Locate platelets.
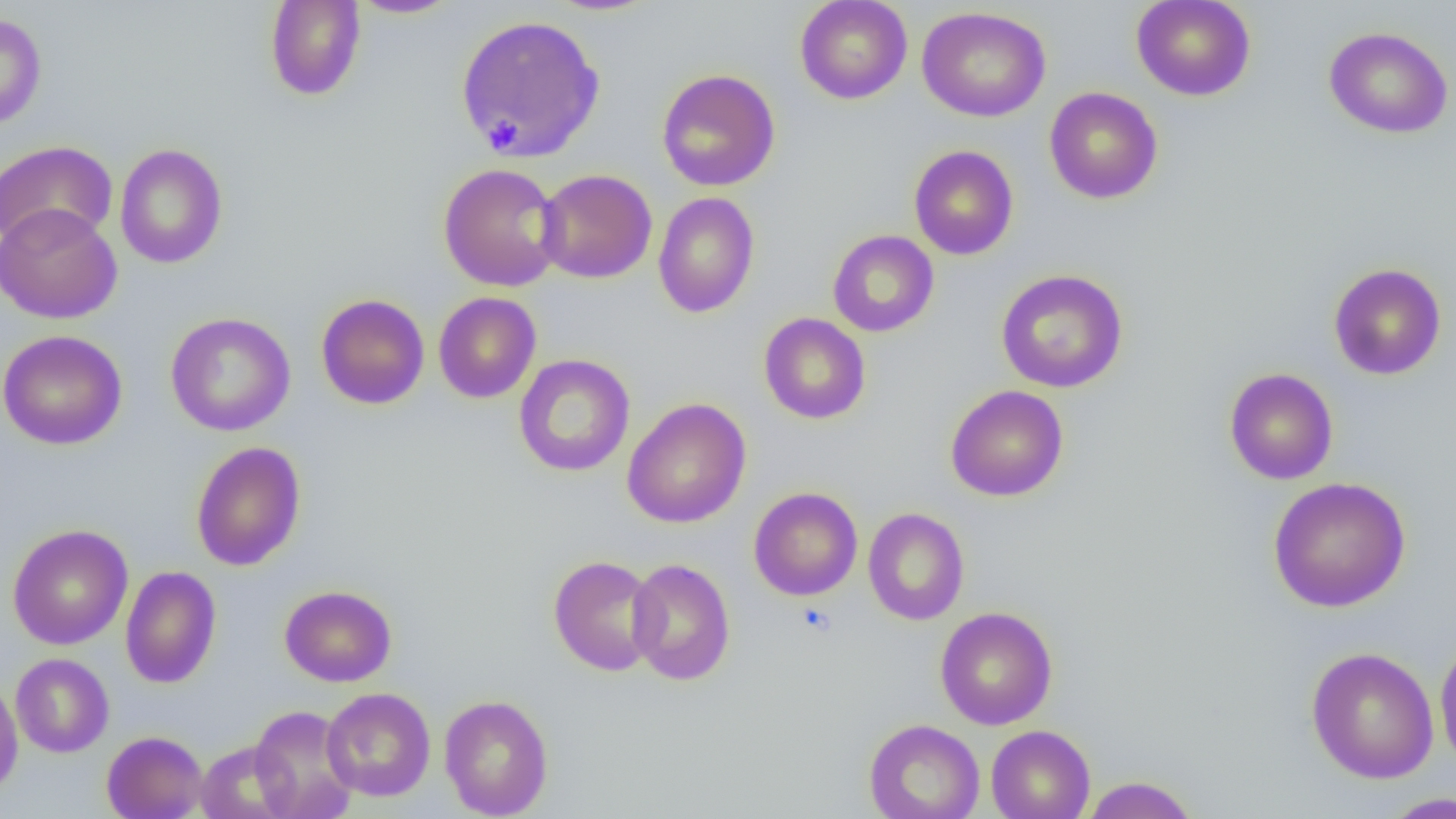
Approximate bounding boxes as named x1/y1/x2/y2 corners in pixels.
Platelets: (x1=488, y1=119, x2=521, y2=152), (x1=796, y1=602, x2=837, y2=636).

Summary:
  - Uninfected red blood cell locations: (x1=265, y1=0, x2=366, y2=101), (x1=349, y1=0, x2=460, y2=19), (x1=795, y1=0, x2=912, y2=104), (x1=1131, y1=0, x2=1256, y2=101), (x1=917, y1=6, x2=1051, y2=122), (x1=0, y1=12, x2=46, y2=130), (x1=454, y1=14, x2=606, y2=163), (x1=1324, y1=26, x2=1453, y2=138), (x1=657, y1=68, x2=780, y2=191), (x1=1044, y1=86, x2=1163, y2=204), (x1=0, y1=140, x2=118, y2=249), (x1=114, y1=143, x2=228, y2=269), (x1=909, y1=144, x2=1019, y2=260), (x1=438, y1=163, x2=565, y2=292), (x1=535, y1=169, x2=657, y2=284), (x1=653, y1=191, x2=759, y2=318), (x1=0, y1=204, x2=122, y2=324), (x1=827, y1=230, x2=939, y2=337), (x1=1328, y1=263, x2=1446, y2=380), (x1=995, y1=268, x2=1128, y2=393), (x1=433, y1=291, x2=541, y2=404), (x1=316, y1=294, x2=430, y2=410), (x1=165, y1=312, x2=296, y2=436), (x1=759, y1=312, x2=871, y2=425), (x1=0, y1=329, x2=127, y2=450), (x1=513, y1=353, x2=635, y2=477), (x1=1224, y1=368, x2=1339, y2=485), (x1=945, y1=385, x2=1069, y2=502), (x1=622, y1=397, x2=751, y2=529), (x1=190, y1=441, x2=306, y2=571), (x1=1268, y1=476, x2=1411, y2=613), (x1=748, y1=487, x2=862, y2=601), (x1=863, y1=507, x2=969, y2=625), (x1=7, y1=524, x2=133, y2=650), (x1=548, y1=555, x2=662, y2=676), (x1=626, y1=558, x2=736, y2=685), (x1=120, y1=565, x2=222, y2=688), (x1=279, y1=584, x2=397, y2=686), (x1=934, y1=606, x2=1058, y2=730), (x1=1434, y1=636, x2=1456, y2=770), (x1=1306, y1=646, x2=1439, y2=784), (x1=10, y1=652, x2=114, y2=758), (x1=0, y1=676, x2=23, y2=799), (x1=322, y1=687, x2=436, y2=801), (x1=439, y1=694, x2=554, y2=818), (x1=249, y1=705, x2=360, y2=819), (x1=864, y1=718, x2=985, y2=819), (x1=985, y1=725, x2=1095, y2=819), (x1=102, y1=730, x2=208, y2=819), (x1=195, y1=740, x2=296, y2=819), (x1=1080, y1=776, x2=1200, y2=819), (x1=1382, y1=792, x2=1456, y2=818)
  - Slide-level diagnosis: no evidence of blood parasites
  - Modality: light microscopy
  - Image size: 1456×819 pixels
  - Magnification: 1000x
  - Field of view: one of a larger specimen
  - Preparation: thin blood film